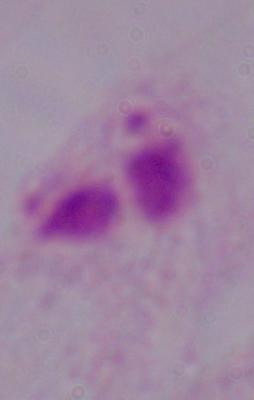
Summary:
  - Magnification: 1000x
  - Modality: photomicrograph
  - Identification: trichomonad